Assess this cell for malaria.
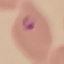
Parasitized.

Giemsa stain. Thin blood smear. Photographed with a smartphone camera at the microscope eyepiece. Automatically extracted cell patch, resized to 64 × 64 pixels.